State which cell type is depicted.
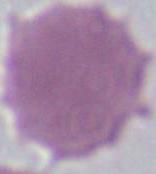

An erythrocyte.

magnification: 1000x
modality: photomicrograph